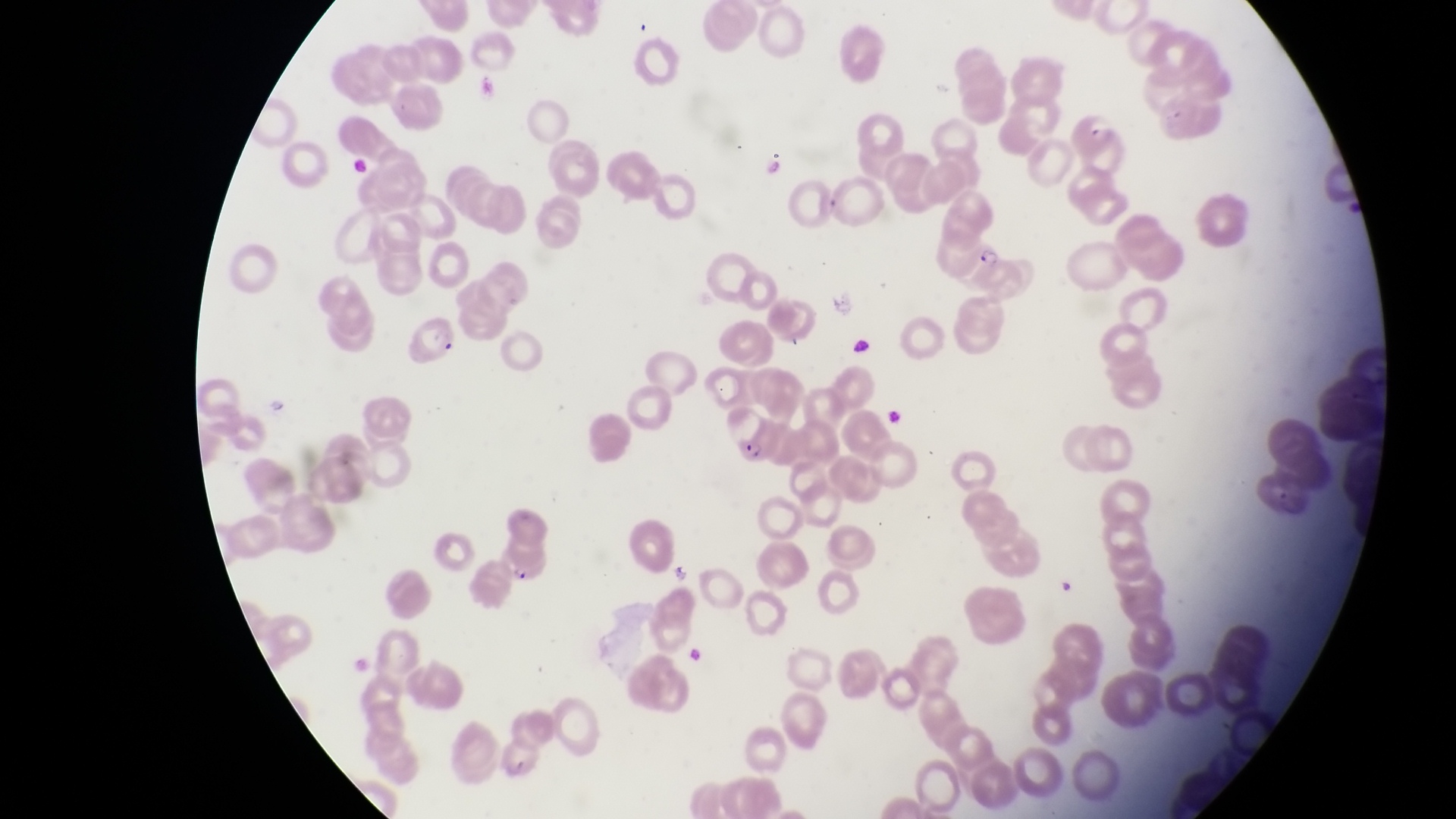 Approximate bounding boxes as [left, top, right, bottom] in pixels. Parasitised red blood cell locations: [1070, 109, 1116, 155], [978, 245, 1039, 301], [419, 323, 461, 362], [733, 416, 783, 471], [497, 547, 544, 584]. Artifact (platelet-like body, stain precipitate, or debris) locations: [838, 336, 877, 359], [885, 402, 904, 434]. One field of view. Magnification of 1000x. Collected in Uganda. Thin blood film. Image is 1456×819 pixels. Captured by a smartphone held over the eyepiece of an Olympus CX-23 microscope.